Name the parasite shown.
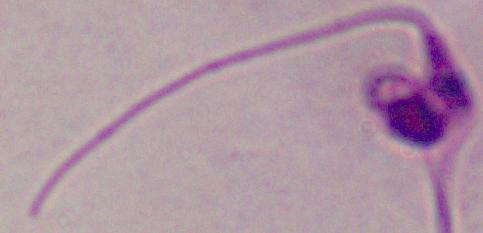
Leishmania.

Summary:
  - Modality: micrograph
  - Magnification: 1000x